Outline each Plasmodium falciparum-infected red blood cell.
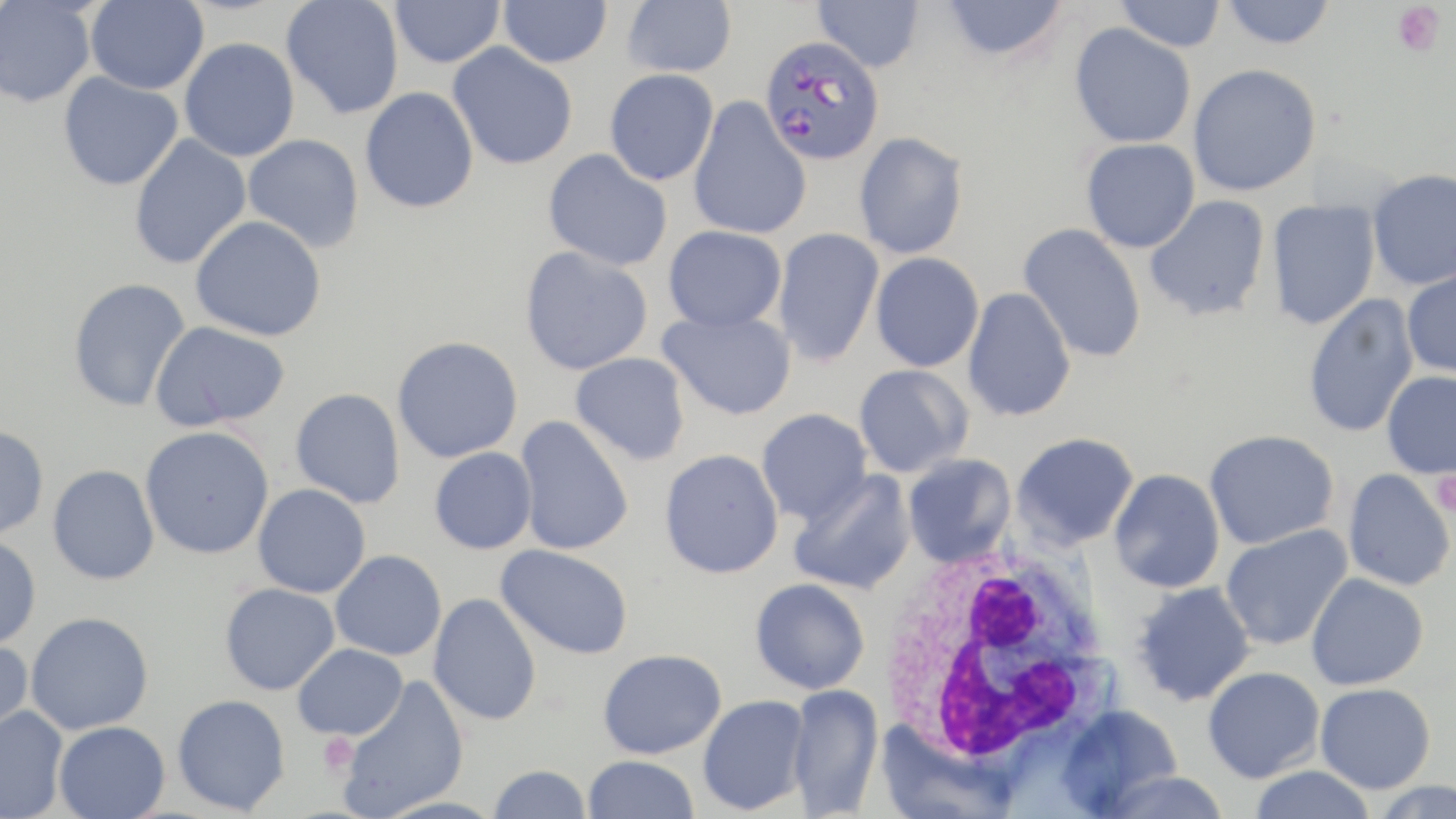

Approximate bounding boxes as [x1, y1, x2, y2] in pixels.
Plasmodium falciparum-infected red blood cells: [759, 35, 885, 166].

Summary:
  - Platelet locations: [1391, 2, 1447, 57], [1432, 470, 1456, 518], [317, 731, 360, 777]
  - White blood cell locations: [872, 537, 1117, 770]
  - Uninfected red blood cell locations: [85, 0, 208, 95], [281, 0, 404, 119], [390, 0, 505, 69], [499, 0, 612, 68], [621, 0, 736, 77], [812, 0, 925, 73], [940, 0, 1069, 62], [1115, 0, 1226, 52], [1221, 0, 1336, 49], [0, 1, 97, 107], [1069, 23, 1197, 149], [179, 37, 300, 162], [448, 42, 578, 169], [1188, 64, 1321, 196], [604, 69, 718, 186], [58, 72, 183, 191], [360, 87, 479, 213], [688, 97, 812, 240], [853, 131, 969, 260], [128, 134, 252, 270], [242, 134, 365, 253], [1081, 138, 1200, 252], [544, 149, 673, 270], [1366, 168, 1456, 290], [1144, 194, 1271, 323], [1266, 199, 1381, 330], [191, 215, 327, 341], [1018, 223, 1147, 363], [663, 225, 786, 332], [772, 227, 884, 368], [519, 246, 653, 375], [870, 252, 985, 372], [1402, 266, 1456, 378], [67, 277, 191, 412], [962, 287, 1076, 423], [1303, 293, 1419, 439], [658, 309, 796, 420], [150, 321, 291, 432], [392, 335, 523, 462], [570, 352, 691, 465], [853, 364, 974, 478], [1381, 371, 1456, 479], [290, 388, 406, 508], [756, 408, 873, 526], [514, 416, 634, 556], [0, 425, 49, 540], [140, 426, 275, 559], [1204, 429, 1339, 550], [1011, 431, 1139, 549], [429, 447, 537, 554], [659, 448, 784, 578], [901, 453, 1017, 567], [47, 464, 160, 585], [1109, 468, 1225, 593], [1342, 469, 1455, 592], [788, 470, 916, 595], [253, 484, 371, 598], [1220, 523, 1353, 651], [0, 534, 41, 650], [495, 544, 634, 660], [330, 550, 447, 661], [1306, 573, 1429, 691], [749, 578, 870, 694], [1131, 581, 1256, 707], [220, 582, 340, 695], [428, 593, 542, 726], [26, 612, 154, 734], [0, 638, 34, 747], [293, 644, 408, 740], [598, 648, 726, 758], [1203, 666, 1325, 783], [335, 674, 470, 819], [786, 683, 884, 817], [1315, 683, 1436, 793], [172, 694, 291, 815], [697, 695, 810, 815], [1056, 704, 1184, 816], [0, 706, 68, 819], [54, 721, 170, 819], [875, 723, 1016, 818], [582, 754, 700, 818], [488, 764, 592, 819], [1249, 766, 1376, 819], [1100, 771, 1231, 818], [1369, 780, 1456, 819]
  - Slide-level diagnosis: Plasmodium falciparum
  - Field of view: one of a larger specimen
  - Preparation: thin blood smear
  - Image size: 1456×819 pixels
  - Stain: May-Grünwald-Giemsa
  - Magnification: 1000x
  - Modality: optical microscopy